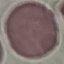

Summary:
  - Result: no malaria parasites seen
  - Capture: smartphone camera at the microscope eyepiece
  - Preparation: thin smear
  - Stain: Giemsa
  - Image type: automatically extracted cell patch, resized to 64 × 64 pixels